Identify the cell.
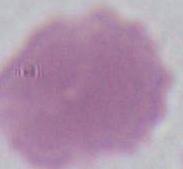

An erythrocyte.

1000x magnification. Micrograph.